Locate and identify every blood parasite.
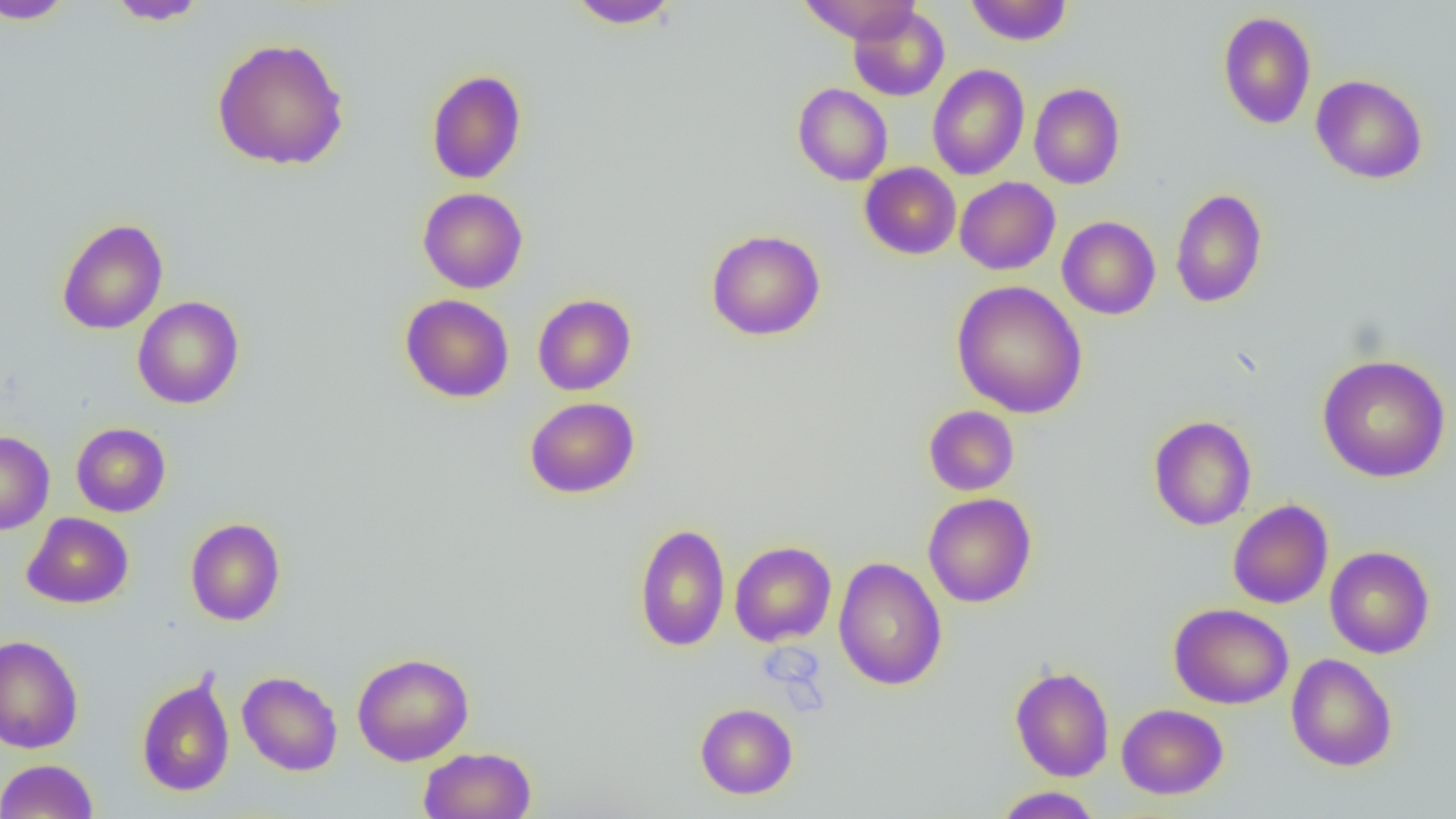
No blood parasites seen.

{
  "slide_level_diagnosis": "no evidence of blood parasites",
  "magnification": "1000x",
  "preparation": "thin blood film",
  "modality": "light microscopy",
  "uninfected_red_blood_cell_locations": "approximate bounding boxes as (x1, y1, x2, y2) in pixels: (0, 0, 76, 25), (567, 0, 681, 29), (798, 0, 921, 43), (965, 0, 1072, 46), (107, 1, 209, 26), (848, 6, 950, 102), (1217, 11, 1317, 129), (211, 37, 350, 170), (927, 64, 1029, 180), (426, 69, 527, 184), (1311, 74, 1428, 184), (793, 83, 893, 185), (1029, 83, 1125, 189), (859, 162, 961, 259), (955, 177, 1060, 275), (418, 187, 528, 293), (1170, 188, 1268, 308), (1057, 216, 1160, 320), (56, 218, 168, 335), (706, 229, 825, 341), (951, 280, 1088, 418), (400, 294, 514, 403), (533, 294, 636, 395), (132, 296, 244, 409), (1317, 353, 1452, 483), (524, 396, 640, 498), (923, 405, 1020, 495), (1148, 415, 1257, 530), (72, 422, 171, 517), (0, 431, 54, 534), (923, 492, 1037, 608), (1228, 499, 1333, 609), (22, 512, 134, 609), (185, 517, 286, 626), (634, 522, 730, 652), (729, 541, 837, 646), (1325, 546, 1435, 658), (730, 549, 947, 662), (833, 557, 947, 691), (1169, 602, 1294, 709), (0, 635, 84, 753), (352, 652, 474, 766), (1285, 653, 1397, 771), (1010, 665, 1114, 782), (237, 671, 343, 776), (136, 672, 235, 797), (695, 702, 797, 799), (1117, 704, 1228, 799), (419, 746, 537, 819), (0, 759, 99, 818), (993, 787, 1102, 818)",
  "image_size": "1456×819 pixels",
  "field_of_view": "single"
}